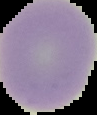

Summary:
  - Preparation: thin blood smear
  - Result: no malaria parasites seen
  - Image size: 97×115 pixels
  - Image type: cell region segmented out of the field of view; surrounding area masked to black